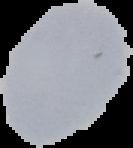

result: no malaria parasites detected
image_size: 133×148 pixels
preparation: thin blood smear
image_type: cell region segmented out of the field of view; surrounding area masked to black